Comment on the morphology of the erythrocytes.
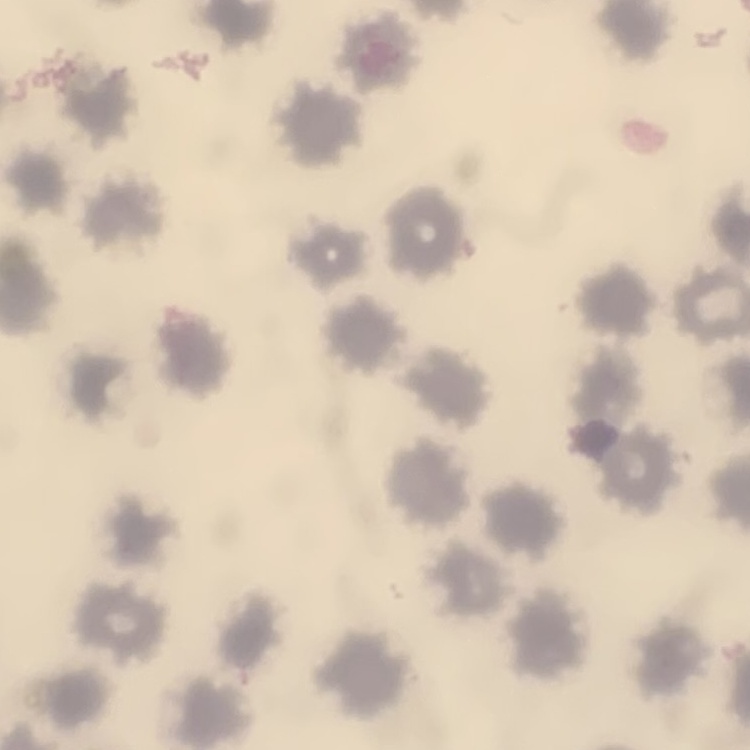

No rouleaux formation.

One tile cut from a larger photomicrograph. Field's or Giemsa stain. Thin blood film.